Give the extent of all uninfected red blood cells.
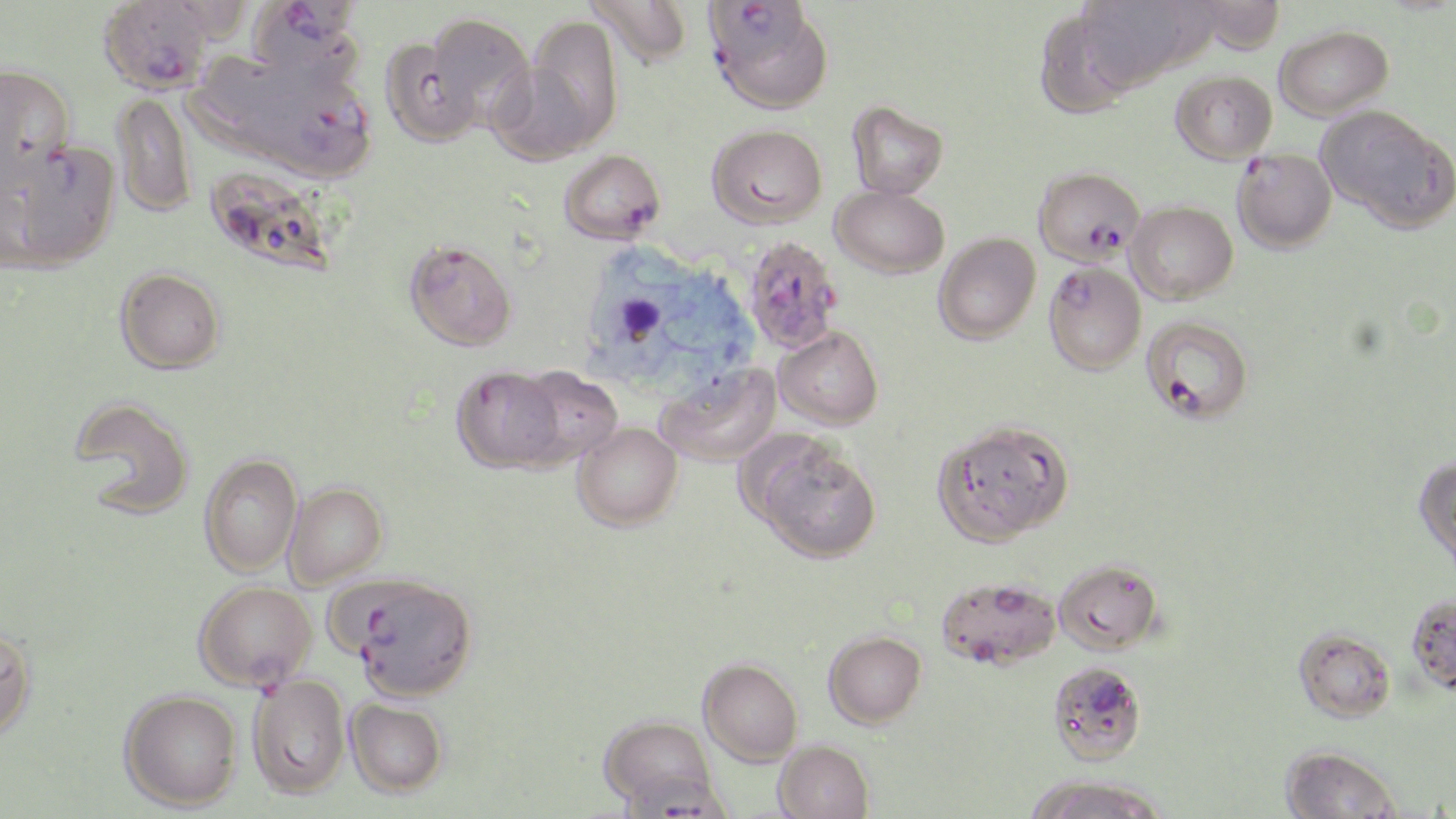
Approximate bounding boxes as named x1/y1/x2/y2 corners in pixels.
Uninfected red blood cells: (x1=586, y1=0, x2=693, y2=68), (x1=1140, y1=0, x2=1228, y2=73), (x1=1078, y1=2, x2=1176, y2=87), (x1=1206, y1=2, x2=1294, y2=56), (x1=424, y1=13, x2=536, y2=132), (x1=521, y1=14, x2=623, y2=152), (x1=1034, y1=23, x2=1134, y2=117), (x1=1275, y1=25, x2=1394, y2=120), (x1=379, y1=35, x2=482, y2=147), (x1=192, y1=59, x2=296, y2=156), (x1=0, y1=63, x2=76, y2=178), (x1=1171, y1=70, x2=1277, y2=164), (x1=112, y1=92, x2=197, y2=218), (x1=846, y1=100, x2=948, y2=199), (x1=1318, y1=105, x2=1455, y2=232), (x1=707, y1=124, x2=827, y2=227), (x1=209, y1=174, x2=333, y2=278), (x1=832, y1=186, x2=949, y2=278), (x1=1125, y1=201, x2=1238, y2=303), (x1=934, y1=232, x2=1041, y2=343), (x1=404, y1=239, x2=518, y2=351), (x1=114, y1=267, x2=226, y2=374), (x1=774, y1=326, x2=883, y2=430), (x1=656, y1=363, x2=781, y2=467), (x1=450, y1=365, x2=563, y2=473), (x1=512, y1=365, x2=622, y2=468), (x1=69, y1=396, x2=195, y2=518), (x1=934, y1=419, x2=1074, y2=544), (x1=573, y1=422, x2=683, y2=531), (x1=751, y1=436, x2=881, y2=563), (x1=199, y1=453, x2=302, y2=577), (x1=1413, y1=454, x2=1456, y2=575), (x1=283, y1=482, x2=388, y2=588), (x1=1054, y1=559, x2=1162, y2=654), (x1=936, y1=575, x2=1060, y2=669), (x1=1405, y1=592, x2=1456, y2=695), (x1=0, y1=624, x2=38, y2=740), (x1=1294, y1=627, x2=1396, y2=723), (x1=823, y1=630, x2=926, y2=727), (x1=699, y1=657, x2=803, y2=764), (x1=247, y1=675, x2=350, y2=798), (x1=119, y1=689, x2=242, y2=810), (x1=346, y1=698, x2=448, y2=797), (x1=598, y1=713, x2=718, y2=812), (x1=774, y1=740, x2=874, y2=819), (x1=1280, y1=743, x2=1403, y2=819), (x1=1022, y1=775, x2=1169, y2=819).

Plasmodium falciparum-infected red blood cell locations: (x1=98, y1=0, x2=216, y2=94), (x1=247, y1=1, x2=364, y2=78), (x1=705, y1=2, x2=809, y2=60), (x1=713, y1=31, x2=833, y2=113), (x1=241, y1=69, x2=373, y2=179), (x1=6, y1=140, x2=121, y2=269), (x1=559, y1=149, x2=665, y2=244), (x1=1232, y1=149, x2=1336, y2=253), (x1=1033, y1=166, x2=1144, y2=266), (x1=748, y1=243, x2=842, y2=355), (x1=1043, y1=262, x2=1146, y2=374), (x1=1141, y1=315, x2=1254, y2=423), (x1=343, y1=575, x2=478, y2=702), (x1=193, y1=580, x2=317, y2=701), (x1=1048, y1=660, x2=1146, y2=765). Slide-level diagnosis: Plasmodium falciparum. May-Grünwald-Giemsa stain. Optical microscopy. Image is 1456×819 pixels. 1000x magnification. One field of a larger specimen. Thin blood film.